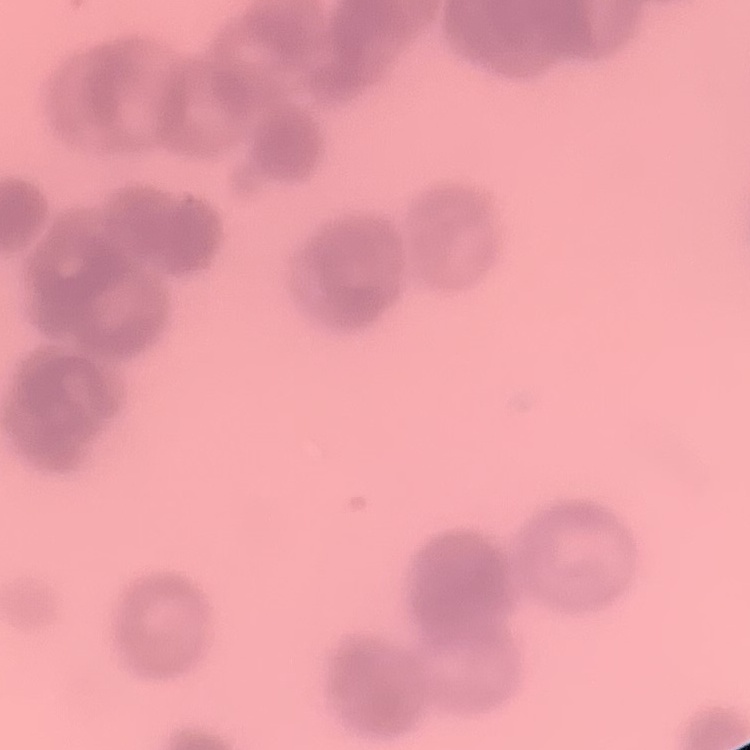
Summary:
  - Erythrocyte morphology: rouleaux formation
  - Image type: square crop of a larger photomicrograph
  - Preparation: thin blood film
  - Stain: Field's or Giemsa